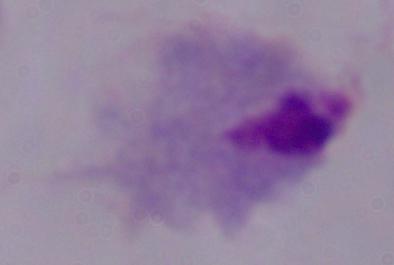
{
  "magnification": "1000x",
  "identification": "trichomonad",
  "modality": "photomicrograph"
}